Assess this cell for malaria.
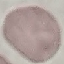
Uninfected.

Thin blood smear. Photographed with a smartphone camera at the microscope eyepiece. Giemsa stain. Automatically extracted cell patch, resized to 64 × 64 pixels.